Identify the blood parasite species.
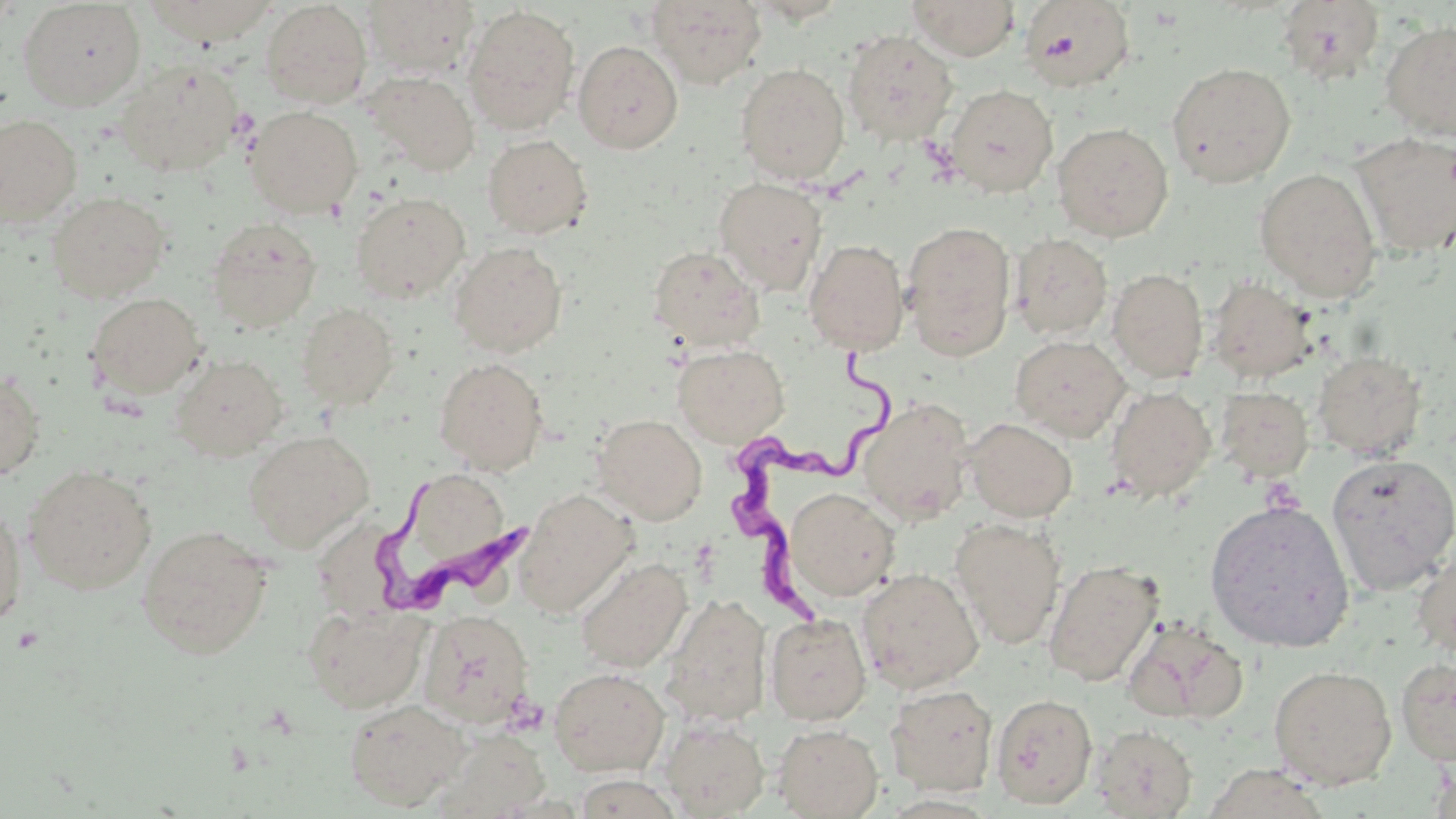

Trypanosoma brucei.

stain = May-Grünwald-Giemsa
uninfected red blood cell locations = approximate bounding boxes as [x1, y1, x2, y2] in pixels: [142, 0, 279, 46], [362, 0, 480, 78], [646, 0, 767, 88], [907, 0, 1020, 60], [1019, 0, 1136, 92], [18, 1, 147, 110], [260, 1, 372, 108], [1276, 1, 1385, 84], [0, 2, 21, 33], [462, 4, 581, 135], [1379, 19, 1456, 140], [842, 29, 959, 147], [573, 40, 683, 153], [117, 60, 244, 177], [1167, 61, 1296, 188], [735, 62, 851, 185], [363, 71, 480, 177], [944, 83, 1058, 197], [245, 106, 363, 218], [0, 114, 83, 227], [1052, 122, 1174, 242], [1351, 132, 1455, 256], [482, 133, 593, 239], [1255, 168, 1382, 300], [713, 176, 828, 295], [350, 191, 470, 303], [46, 192, 171, 302], [205, 217, 322, 333], [901, 220, 1016, 361], [1010, 233, 1113, 340], [803, 239, 910, 355], [449, 241, 567, 357], [647, 245, 764, 351], [1108, 268, 1209, 382], [1206, 276, 1317, 383], [87, 292, 207, 399], [296, 303, 398, 410], [1010, 334, 1130, 441], [672, 343, 790, 447], [1312, 350, 1427, 460], [170, 353, 288, 461], [434, 357, 549, 474], [0, 370, 45, 480], [1105, 385, 1217, 502], [1216, 386, 1314, 482], [858, 398, 974, 523], [592, 414, 707, 525], [964, 418, 1078, 522], [243, 430, 374, 551], [1327, 452, 1456, 595], [24, 465, 156, 595], [414, 478, 504, 556], [784, 487, 899, 601], [514, 489, 637, 618], [1204, 498, 1355, 653], [0, 503, 27, 629], [950, 518, 1066, 650], [137, 525, 273, 659], [1412, 543, 1456, 661], [574, 557, 692, 672], [1044, 559, 1163, 687], [857, 567, 984, 693], [661, 594, 772, 727], [303, 605, 428, 713], [419, 610, 534, 730], [765, 613, 872, 725], [1122, 617, 1249, 726], [1395, 656, 1456, 767], [1268, 664, 1397, 790], [549, 667, 670, 776], [885, 684, 998, 796], [990, 693, 1097, 809], [343, 697, 469, 810], [661, 719, 769, 818], [773, 723, 883, 818], [1092, 724, 1199, 818], [437, 730, 550, 818], [1199, 763, 1332, 819], [572, 772, 682, 818]
image size = 1456×819 pixels
preparation = thin blood film
field of view = single
Trypanosoma brucei locations = approximate bounding boxes as [x1, y1, x2, y2] in pixels: [732, 344, 913, 636], [380, 486, 536, 615]
magnification = 1000x
platelet locations = approximate bounding boxes as [x1, y1, x2, y2] in pixels: [11, 626, 44, 654]
modality = light microscopy